Mark where platelets are.
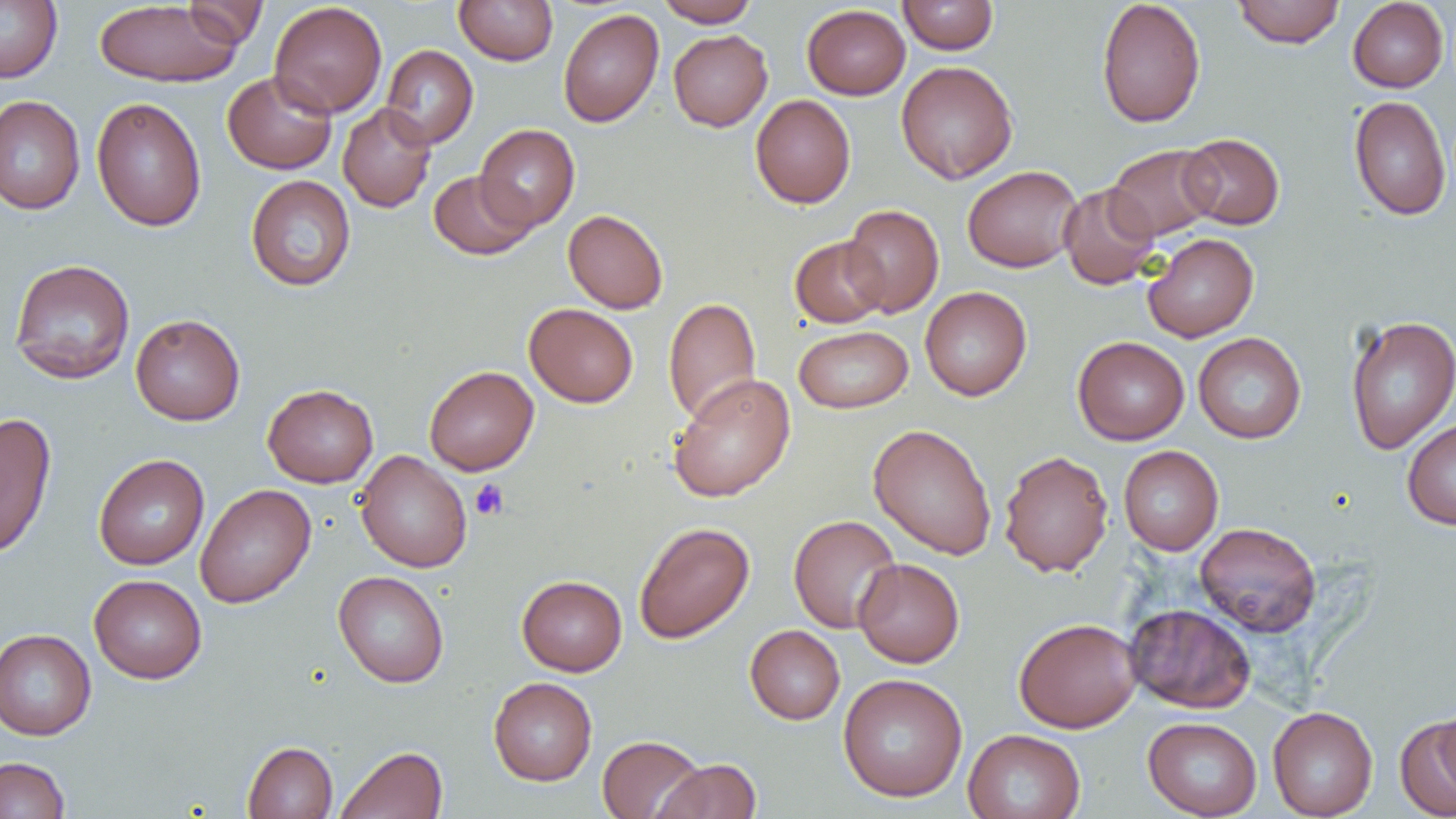
Approximate bounding boxes as (x1, y1, x2, y2) in pixels.
Platelets: (470, 479, 509, 521).

Summary:
  - Uninfected red blood cell locations: (454, 0, 558, 66), (656, 0, 759, 27), (1096, 0, 1206, 128), (1232, 0, 1345, 48), (1347, 0, 1448, 92), (0, 1, 62, 82), (94, 1, 244, 88), (182, 1, 268, 48), (269, 1, 387, 118), (898, 1, 999, 55), (802, 4, 910, 99), (558, 8, 663, 127), (669, 30, 772, 131), (381, 45, 478, 149), (896, 60, 1018, 184), (223, 70, 337, 174), (750, 94, 856, 208), (0, 95, 85, 215), (1348, 95, 1452, 221), (91, 97, 207, 232), (337, 103, 436, 213), (475, 124, 580, 230), (1180, 132, 1284, 230), (1105, 144, 1221, 242), (962, 165, 1083, 272), (428, 170, 538, 260), (245, 174, 356, 292), (1058, 183, 1160, 290), (842, 204, 944, 317), (563, 209, 668, 313), (1143, 233, 1259, 342), (790, 236, 889, 328), (9, 258, 135, 384), (920, 286, 1032, 401), (663, 297, 762, 425), (524, 303, 638, 407), (130, 314, 245, 426), (1344, 314, 1456, 454), (793, 325, 913, 413), (1193, 332, 1307, 444), (1073, 336, 1189, 445), (424, 365, 539, 475), (668, 373, 795, 503), (263, 384, 378, 487), (0, 412, 56, 560), (1402, 419, 1456, 531), (868, 423, 996, 560), (1118, 446, 1223, 555), (998, 450, 1113, 577), (355, 451, 473, 573), (94, 454, 209, 569), (195, 484, 316, 608), (788, 514, 902, 633), (633, 521, 754, 643), (1194, 522, 1322, 636), (853, 558, 965, 667), (333, 571, 449, 687), (89, 574, 207, 684), (517, 575, 627, 676), (1125, 603, 1255, 713), (1014, 617, 1142, 733), (745, 625, 845, 725), (0, 628, 96, 740), (838, 673, 968, 802), (488, 676, 597, 786), (1433, 705, 1455, 798), (1268, 706, 1378, 818), (1395, 715, 1455, 818), (1143, 717, 1262, 818), (963, 728, 1086, 819), (597, 734, 706, 818), (242, 741, 337, 818), (335, 746, 447, 819), (0, 756, 70, 819), (653, 758, 762, 819)
  - Slide-level diagnosis: negative for blood parasites
  - Modality: light microscopy
  - Image size: 1456×819 pixels
  - Magnification: 1000x
  - Preparation: thin blood smear
  - Field of view: single